Locate leukocytes (white blood cells).
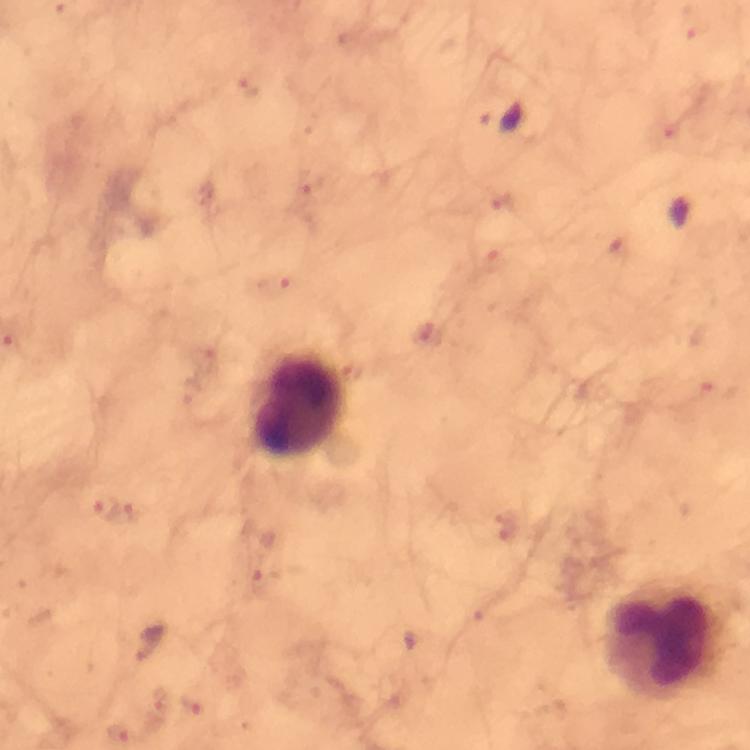

Approximate centers as (x, y) in pixels.
Leukocytes: (300, 404), (664, 640).

cropped from = a single field of view
preparation = thick blood smear
capture = smartphone mounted on the microscope
Plasmodium parasite locations = approximate centers as (x, y) in pixels: (106, 509)
context = from a diagnostic examination for malaria
magnification = 100x
stain = Giemsa
image size = 750×750 pixels
immersion oil = applied